Mark where leukocytes are.
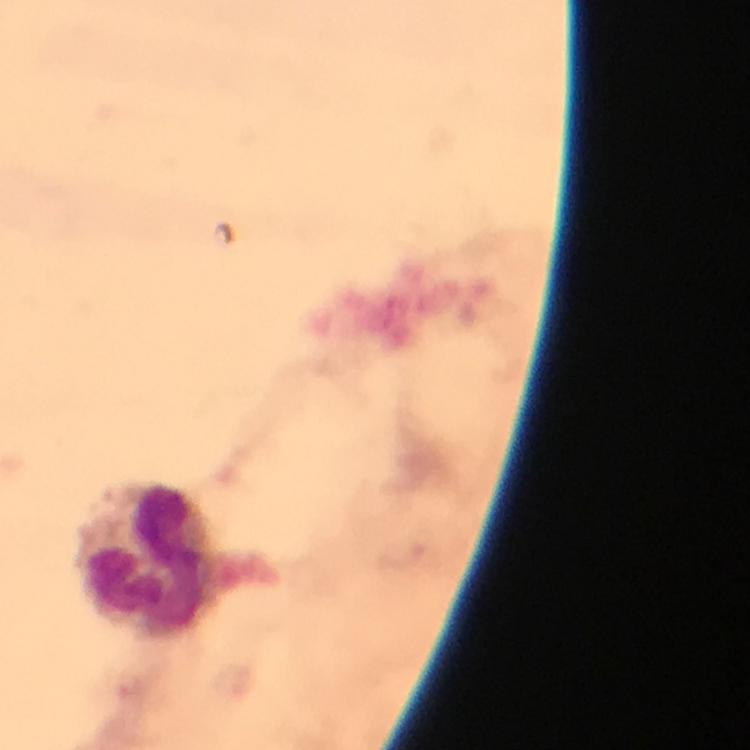
Approximate centers as (x, y) in pixels.
Leukocytes: (148, 559).

cropped from = one field of view
Plasmodium parasites = none detected
preparation = thick blood film
magnification = 100x
capture = smartphone photograph through a microscope
context = from a malaria diagnostic workup
immersion oil = applied
stain = Giemsa
image size = 750×750 pixels